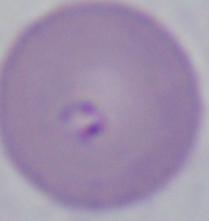
modality = photomicrograph
identification = Babesia
magnification = 1000x